Comment on the morphology of the erythrocytes.
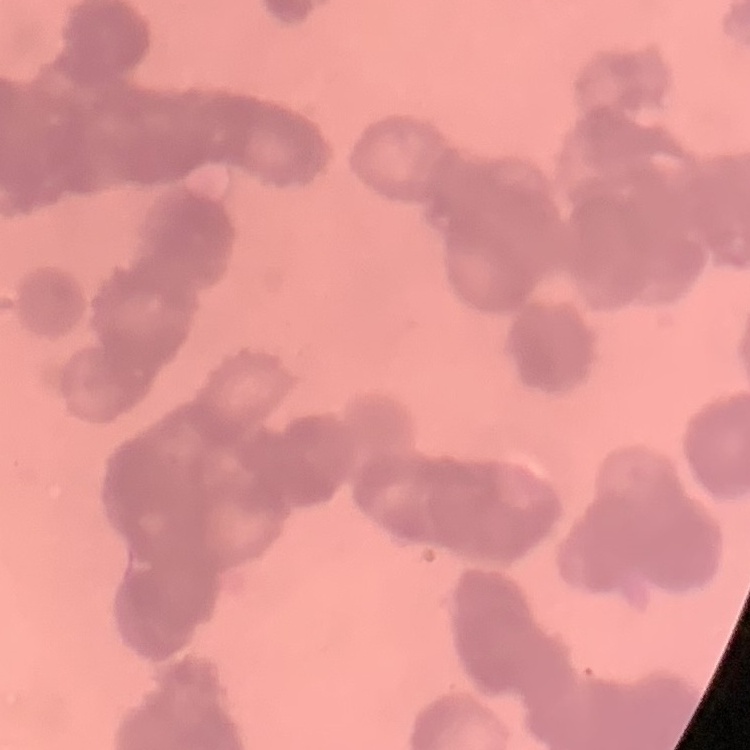
They show rouleaux formation.

Square crop of a larger photomicrograph. Thin blood film. Field's or Giemsa stain.